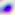

magnification = 400x
modality = micrograph
identification = Toxoplasma gondii